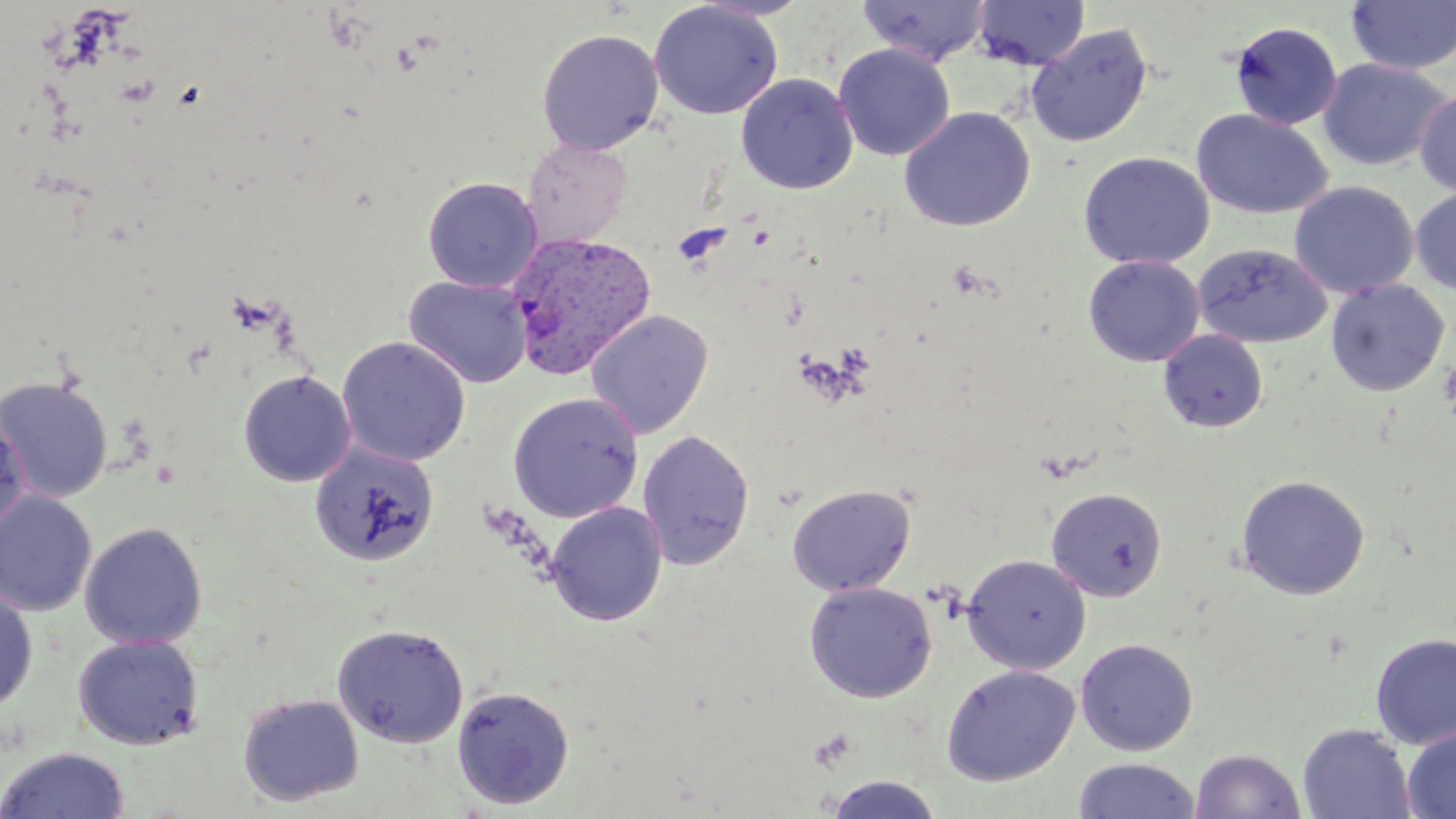

{
  "slide_level_diagnosis": "Plasmodium vivax",
  "modality": "light microscopy",
  "stain": "May-Grünwald-Giemsa",
  "preparation": "thin blood smear",
  "plasmodium_vivax_infected_red_blood_cell_locations": "approximate bounding boxes as named x1/y1/x2/y2 corners in pixels: (x1=506, y1=230, x2=657, y2=380)",
  "magnification": "1000x",
  "image_size": "1456×819 pixels",
  "field_of_view": "one of a larger specimen",
  "platelet_locations": "approximate bounding boxes as named x1/y1/x2/y2 corners in pixels: (x1=946, y1=260, x2=993, y2=300), (x1=836, y1=343, x2=875, y2=375), (x1=1437, y1=360, x2=1456, y2=419), (x1=811, y1=727, x2=858, y2=770)",
  "uninfected_red_blood_cell_locations": "approximate bounding boxes as named x1/y1/x2/y2 corners in pixels: (x1=857, y1=0, x2=993, y2=66), (x1=973, y1=0, x2=1089, y2=71), (x1=649, y1=1, x2=783, y2=120), (x1=1346, y1=1, x2=1456, y2=75), (x1=1229, y1=21, x2=1343, y2=130), (x1=1026, y1=24, x2=1153, y2=149), (x1=537, y1=28, x2=664, y2=155), (x1=834, y1=43, x2=955, y2=161), (x1=1318, y1=58, x2=1451, y2=171), (x1=736, y1=73, x2=858, y2=195), (x1=1415, y1=88, x2=1456, y2=197), (x1=898, y1=106, x2=1035, y2=232), (x1=1192, y1=109, x2=1333, y2=219), (x1=522, y1=138, x2=633, y2=249), (x1=1078, y1=152, x2=1215, y2=270), (x1=422, y1=176, x2=543, y2=292), (x1=1289, y1=181, x2=1418, y2=299), (x1=1410, y1=188, x2=1456, y2=295), (x1=1193, y1=243, x2=1332, y2=348), (x1=1083, y1=255, x2=1205, y2=367), (x1=404, y1=275, x2=533, y2=388), (x1=1326, y1=279, x2=1450, y2=397), (x1=586, y1=310, x2=713, y2=438), (x1=1158, y1=329, x2=1268, y2=433), (x1=336, y1=336, x2=471, y2=466), (x1=238, y1=370, x2=356, y2=487), (x1=0, y1=375, x2=113, y2=503), (x1=508, y1=392, x2=643, y2=523), (x1=0, y1=415, x2=31, y2=534), (x1=637, y1=429, x2=755, y2=569), (x1=309, y1=441, x2=440, y2=568), (x1=1236, y1=475, x2=1370, y2=600), (x1=786, y1=484, x2=916, y2=596), (x1=1046, y1=487, x2=1167, y2=601), (x1=0, y1=490, x2=97, y2=616), (x1=545, y1=502, x2=667, y2=626), (x1=79, y1=521, x2=208, y2=650), (x1=961, y1=554, x2=1092, y2=674), (x1=803, y1=581, x2=938, y2=703), (x1=0, y1=586, x2=38, y2=713), (x1=332, y1=623, x2=468, y2=747), (x1=1371, y1=632, x2=1456, y2=749), (x1=73, y1=633, x2=204, y2=750), (x1=1075, y1=638, x2=1198, y2=756), (x1=941, y1=664, x2=1079, y2=785), (x1=451, y1=684, x2=575, y2=810), (x1=237, y1=692, x2=364, y2=806), (x1=1297, y1=724, x2=1416, y2=819), (x1=1402, y1=727, x2=1456, y2=818), (x1=0, y1=746, x2=131, y2=819), (x1=1190, y1=748, x2=1306, y2=819), (x1=1073, y1=758, x2=1200, y2=818), (x1=821, y1=774, x2=946, y2=818)"
}